Describe the morphology of the erythrocytes.
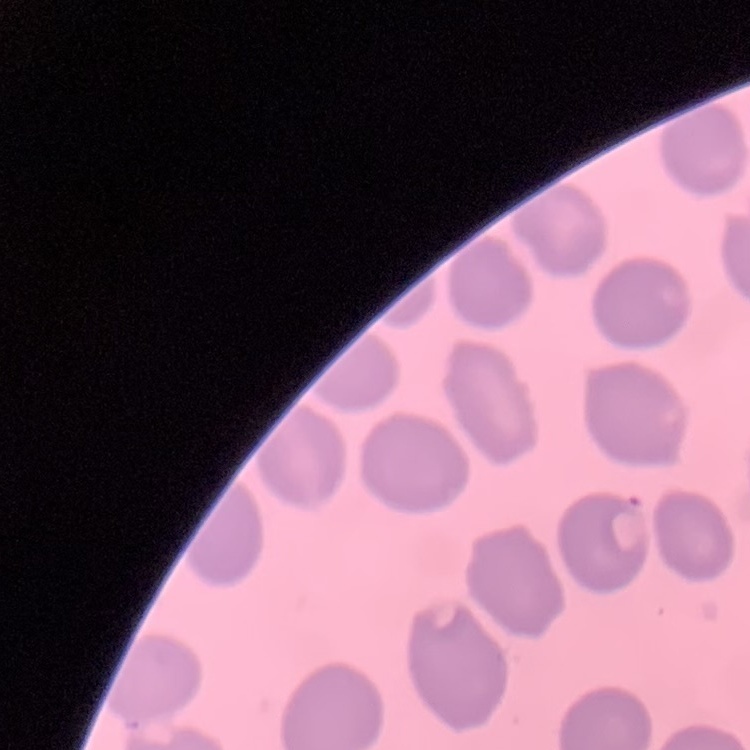
They show no rouleaux formation.

{
  "image_type": "square crop of a larger photomicrograph",
  "preparation": "thin peripheral smear",
  "stain": "Field's or Giemsa"
}